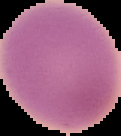

preparation: thin blood film
image_type: segmented cell region on a black background
image_size: 121×136 pixels
result: no Plasmodium parasites detected